Locate every leukocyte (white blood cell).
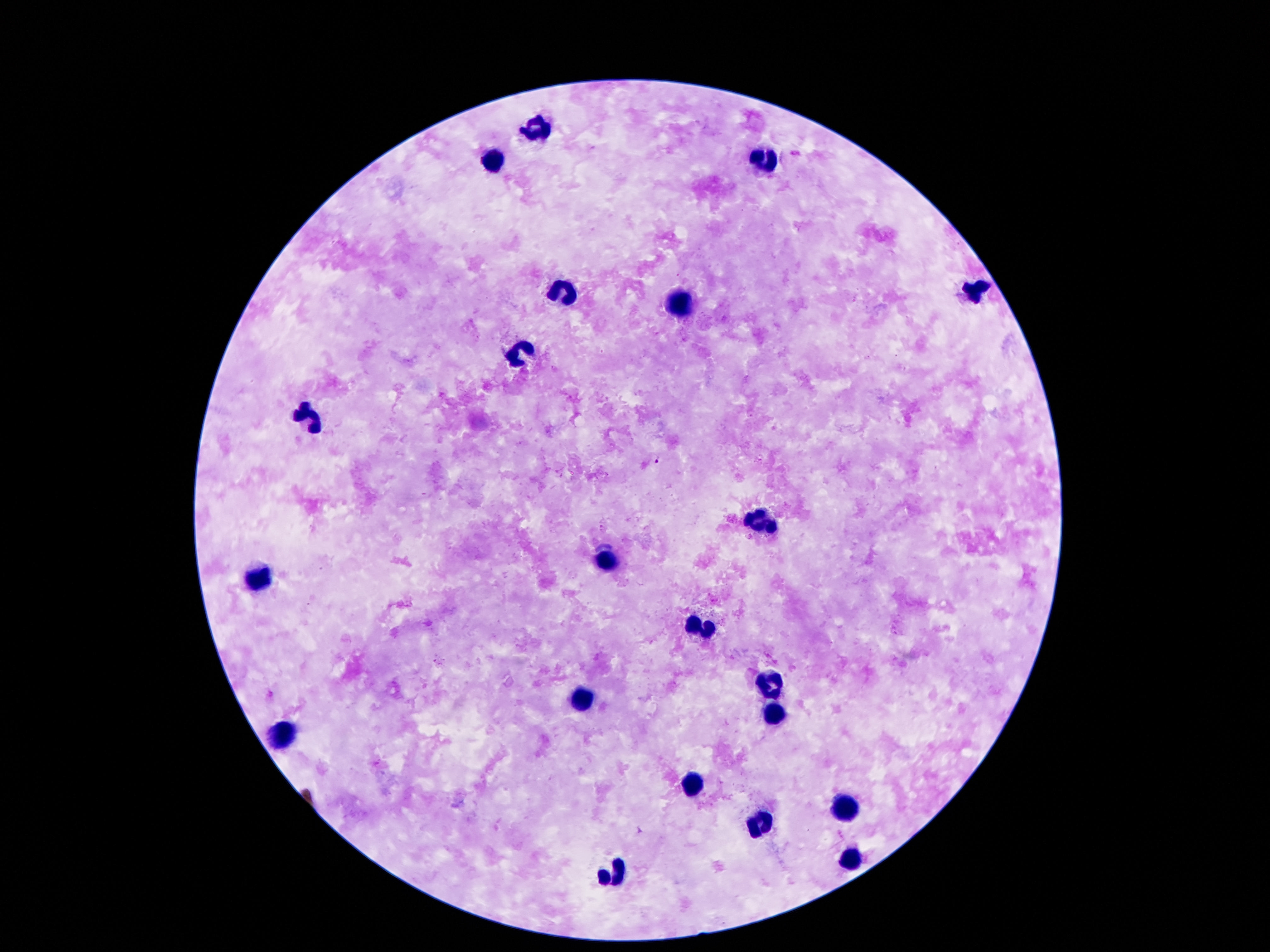
Approximate centers as (x, y) in pixels.
Leukocytes: (534, 129), (768, 161), (493, 164), (976, 289), (561, 291), (679, 304), (520, 350), (310, 416), (758, 520), (609, 561), (258, 578), (698, 627), (770, 686), (585, 698), (775, 714), (284, 733), (694, 781), (843, 809), (762, 825), (851, 861), (613, 874).

Summary:
  - Preparation: thick peripheral-blood smear
  - Image size: 1270×952 pixels
  - Stain: Giemsa
  - Patient malaria status: uninfected
  - Capture: smartphone camera through the microscope eyepiece
  - Field of view: one from this slide
  - Magnification: 100x